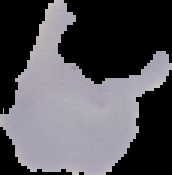
From a thin blood film. Segmented cell region on a black background. Result: malaria parasites detected. Image is 172×175 pixels.